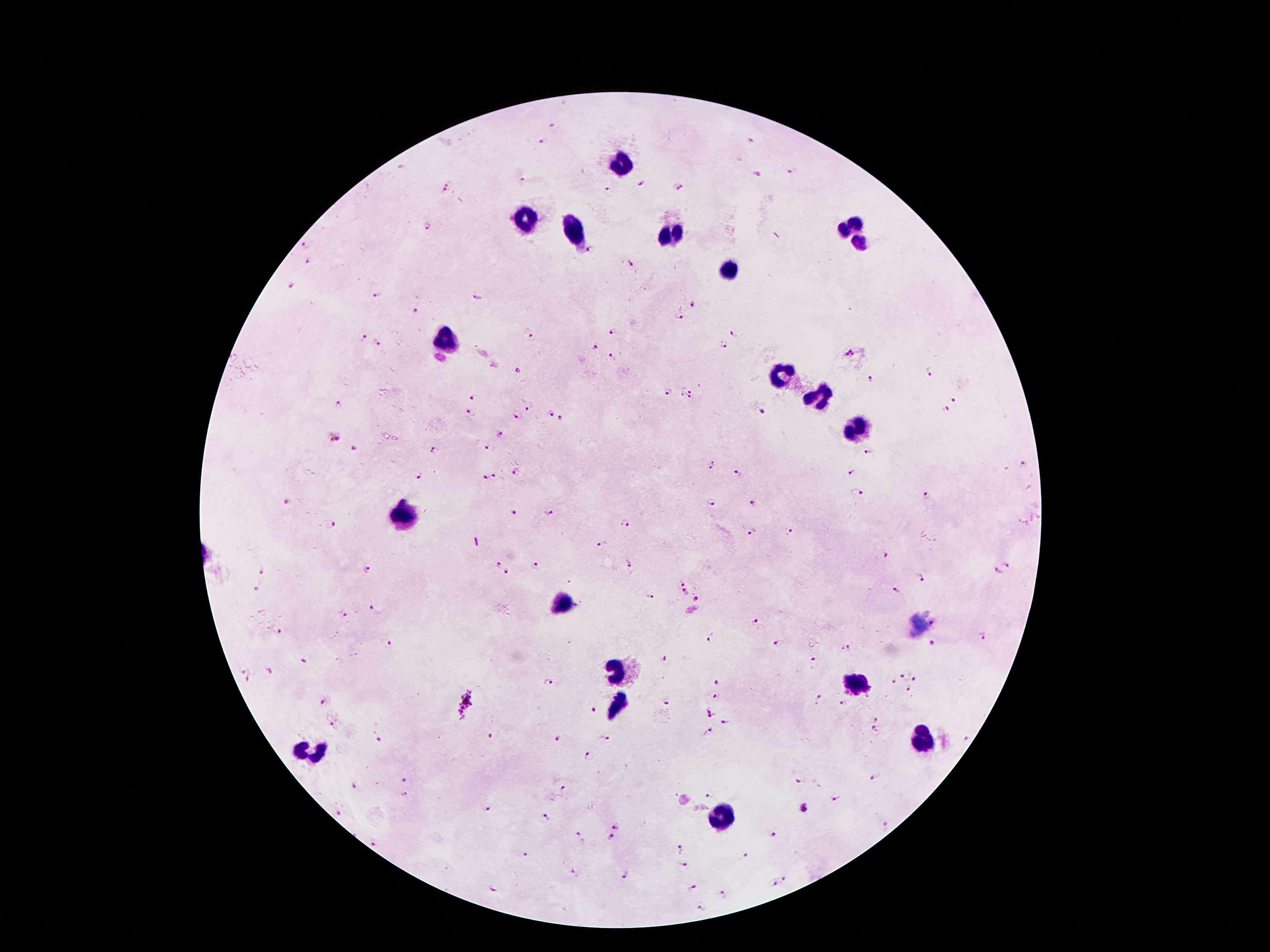
malaria_parasite_locations: 'approximate object centers, in pixels from the top-left corner: (x=552, y=124), (x=749, y=140), (x=541, y=141), (x=401, y=166), (x=792, y=172), (x=755, y=174), (x=522, y=181), (x=638, y=182), (x=680, y=185), (x=446, y=188), (x=609, y=191), (x=428, y=228), (x=307, y=244), (x=590, y=250), (x=310, y=260), (x=630, y=266), (x=292, y=287), (x=377, y=295), (x=476, y=295), (x=694, y=304), (x=414, y=311), (x=678, y=316), (x=612, y=331), (x=528, y=333), (x=733, y=333), (x=364, y=339), (x=377, y=344), (x=723, y=346), (x=595, y=348), (x=851, y=354), (x=609, y=358), (x=517, y=371), (x=931, y=373), (x=872, y=379), (x=669, y=394), (x=687, y=394), (x=474, y=398), (x=956, y=400), (x=338, y=405), (x=531, y=406), (x=948, y=409), (x=761, y=412), (x=471, y=413), (x=551, y=415), (x=519, y=417), (x=561, y=420), (x=500, y=433), (x=336, y=438), (x=354, y=449), (x=436, y=450), (x=488, y=450), (x=870, y=451), (x=711, y=464), (x=1023, y=464), (x=850, y=473), (x=516, y=474), (x=737, y=475), (x=419, y=476), (x=484, y=477), (x=495, y=477), (x=856, y=493), (x=927, y=497), (x=285, y=501), (x=710, y=501), (x=753, y=504), (x=513, y=510), (x=550, y=512), (x=624, y=524), (x=331, y=526), (x=753, y=532), (x=789, y=532), (x=604, y=543), (x=887, y=556), (x=1009, y=562), (x=629, y=564), (x=497, y=565), (x=533, y=567), (x=260, y=568), (x=368, y=568), (x=507, y=571), (x=999, y=574), (x=923, y=579), (x=680, y=582), (x=256, y=588), (x=897, y=590), (x=684, y=593), (x=651, y=596), (x=699, y=599), (x=369, y=607), (x=345, y=615), (x=757, y=619), (x=935, y=619), (x=277, y=632), (x=983, y=635), (x=712, y=638), (x=385, y=643), (x=777, y=643), (x=934, y=643), (x=847, y=646), (x=664, y=657), (x=812, y=660), (x=304, y=661), (x=270, y=671), (x=247, y=676), (x=903, y=676), (x=915, y=678), (x=717, y=680), (x=550, y=683), (x=893, y=683), (x=909, y=691), (x=717, y=696), (x=324, y=701), (x=819, y=701), (x=843, y=703), (x=468, y=704), (x=664, y=704), (x=593, y=710), (x=713, y=712), (x=877, y=718), (x=724, y=721), (x=335, y=723), (x=707, y=729), (x=876, y=731), (x=494, y=736), (x=603, y=738), (x=377, y=739), (x=555, y=739), (x=588, y=756), (x=874, y=776), (x=799, y=781), (x=404, y=782), (x=354, y=786), (x=563, y=791), (x=709, y=793), (x=404, y=795), (x=836, y=797), (x=803, y=807), (x=486, y=809), (x=339, y=814), (x=545, y=817), (x=614, y=825), (x=885, y=826), (x=579, y=835), (x=612, y=835), (x=774, y=835), (x=376, y=844), (x=680, y=850), (x=523, y=853), (x=742, y=854), (x=683, y=865), (x=572, y=873), (x=625, y=875), (x=784, y=878), (x=772, y=884), (x=691, y=887), (x=495, y=888), (x=721, y=895), (x=704, y=908)'
leukocyte_locations: 'approximate object centers, in pixels from the top-left corner: (x=624, y=162), (x=524, y=220), (x=856, y=225), (x=843, y=227), (x=573, y=228), (x=670, y=233), (x=860, y=241), (x=730, y=271), (x=451, y=341), (x=781, y=377), (x=813, y=395), (x=856, y=425), (x=402, y=512), (x=564, y=605), (x=619, y=667), (x=857, y=683), (x=618, y=704), (x=922, y=735), (x=310, y=751), (x=722, y=822)'
preparation: thick blood film
stain: Giemsa
patient_malaria_status: infected with Plasmodium falciparum
magnification: 100x
image_size: 1270×952 pixels
field_of_view: single
capture: smartphone through the microscope eyepiece